Evaluate for Plasmodium parasites.
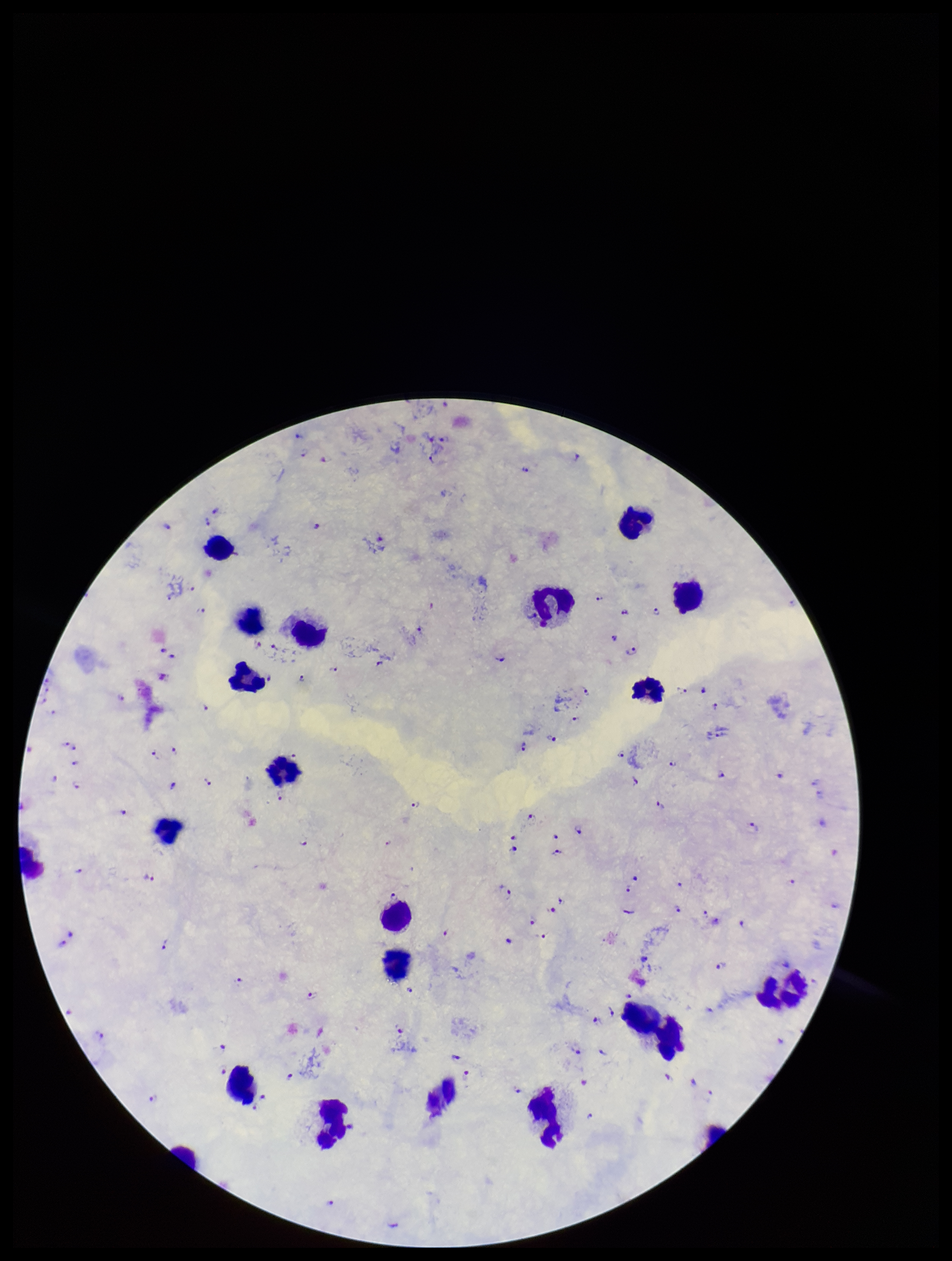

Detected.

Summary:
  - Species reported for this patient: Plasmodium falciparum
  - Preparation: thick smear
  - Image size: 952×1261 pixels
  - Stain: Giemsa
  - Leukocyte count: 21
  - Patient malaria status: positive
  - Field of view: one from this slide
  - Capture: smartphone photograph through the microscope eyepiece
  - Parasite count: 103